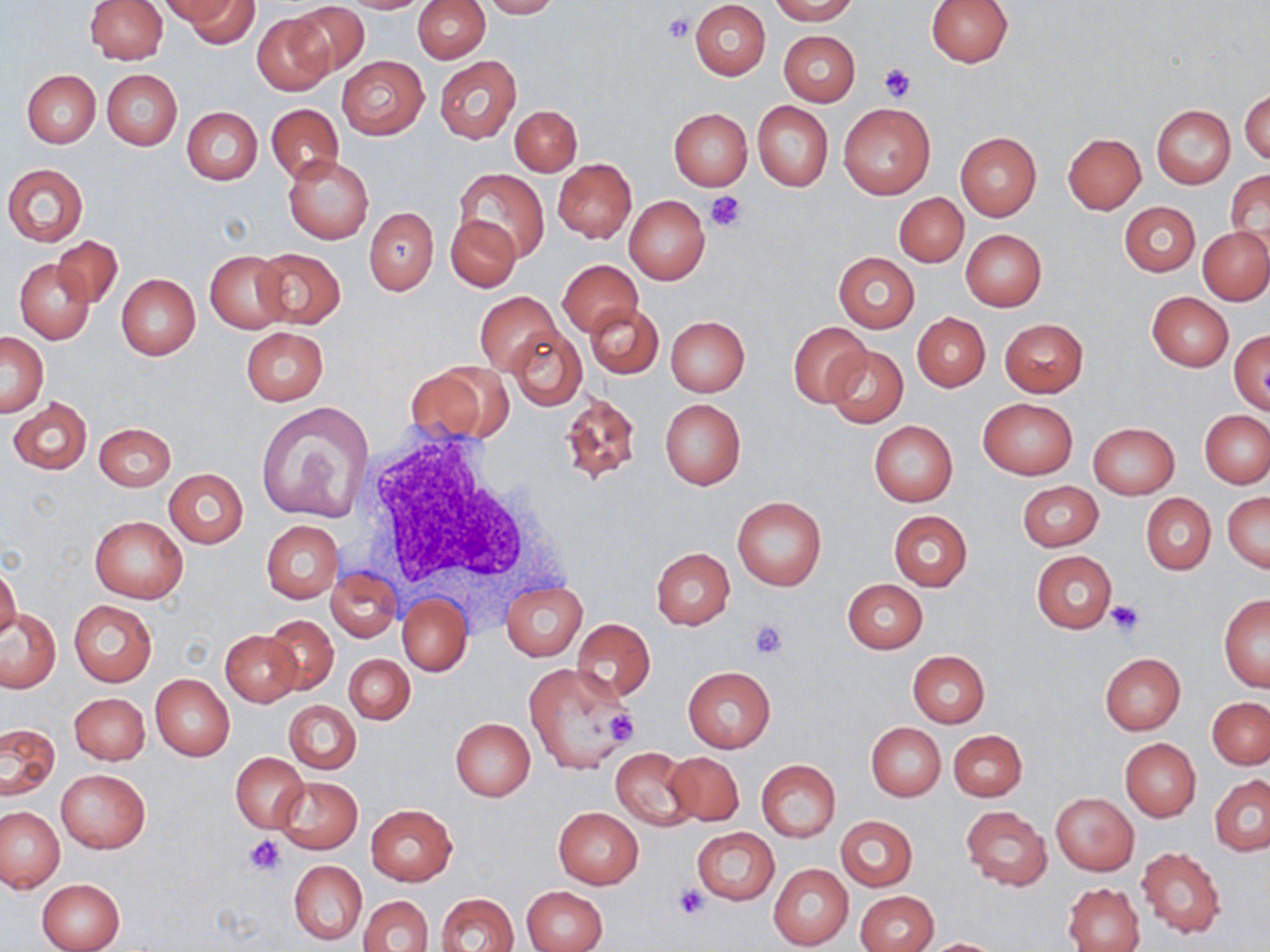

Approximate bounding boxes as (x1, y1, x2, y2) in pixels. White blood cell locations: (359, 428, 543, 607). Uninfected red blood cell locations: (84, 0, 168, 62), (161, 0, 241, 25), (182, 0, 260, 48), (339, 0, 432, 13), (413, 0, 490, 63), (478, 0, 560, 19), (769, 0, 859, 24), (926, 0, 1013, 67), (690, 1, 771, 80), (286, 2, 370, 78), (252, 16, 332, 95), (779, 30, 860, 106), (434, 55, 520, 144), (336, 56, 428, 140), (102, 69, 183, 150), (22, 70, 100, 148), (1240, 88, 1269, 165), (752, 101, 833, 192), (266, 103, 343, 183), (838, 103, 935, 199), (510, 105, 581, 176), (1152, 105, 1234, 189), (182, 107, 262, 185), (669, 108, 751, 190), (955, 132, 1041, 220), (1063, 133, 1145, 214), (282, 152, 374, 244), (552, 159, 636, 243), (3, 163, 89, 246), (454, 169, 549, 261), (1225, 169, 1270, 256), (894, 192, 968, 267), (625, 197, 710, 284), (1120, 201, 1200, 277), (365, 208, 438, 294), (446, 213, 519, 292), (1199, 228, 1270, 304), (961, 229, 1046, 311), (52, 236, 122, 309), (250, 247, 346, 327), (204, 250, 292, 332), (834, 252, 918, 333), (15, 259, 95, 344), (559, 260, 642, 337), (117, 274, 199, 359), (474, 291, 560, 376), (1147, 291, 1234, 371), (585, 304, 663, 378), (912, 314, 990, 390), (665, 315, 751, 396), (1000, 318, 1089, 397), (788, 322, 870, 406), (507, 326, 586, 409), (242, 327, 328, 405), (1229, 330, 1270, 414), (1, 331, 48, 416), (824, 345, 908, 430), (405, 363, 510, 444), (560, 393, 640, 486), (7, 398, 91, 475), (660, 398, 745, 489), (977, 398, 1077, 479), (255, 402, 375, 523), (1200, 411, 1270, 487), (869, 421, 958, 507), (93, 423, 175, 492), (1087, 423, 1179, 500), (164, 468, 248, 547), (1024, 480, 1106, 630), (1017, 481, 1104, 550), (1222, 493, 1269, 572), (1141, 494, 1215, 575), (732, 496, 827, 590), (888, 510, 973, 591), (90, 516, 188, 603), (262, 520, 343, 604), (652, 548, 734, 630), (1032, 551, 1117, 633), (0, 564, 21, 643), (326, 567, 400, 642), (329, 577, 467, 652), (843, 579, 927, 654), (501, 581, 587, 661), (397, 594, 470, 675), (1219, 595, 1270, 690), (69, 600, 157, 687), (0, 608, 60, 692), (263, 614, 339, 696), (571, 619, 656, 701), (220, 629, 299, 705), (907, 650, 990, 727), (345, 653, 415, 725), (1099, 653, 1186, 735), (524, 664, 630, 774), (684, 666, 775, 752), (151, 674, 234, 761), (69, 692, 150, 764), (1208, 698, 1270, 768), (284, 699, 361, 774), (451, 718, 536, 801), (0, 723, 60, 799), (867, 723, 946, 800), (949, 730, 1027, 801), (1120, 738, 1201, 821), (610, 748, 698, 830), (662, 752, 744, 827), (231, 753, 309, 831), (756, 759, 841, 842), (55, 769, 151, 854), (1210, 775, 1270, 855), (274, 776, 363, 853), (1051, 793, 1138, 875), (366, 804, 456, 885), (961, 805, 1052, 891), (0, 806, 66, 893), (553, 807, 643, 888), (836, 816, 918, 890), (691, 827, 779, 904), (1136, 847, 1225, 939), (289, 861, 367, 945), (768, 864, 853, 949), (38, 878, 125, 952), (1063, 882, 1144, 952), (520, 885, 607, 952), (855, 891, 938, 952), (436, 892, 519, 952), (360, 895, 433, 952), (922, 938, 1005, 951). Platelet locations: (665, 13, 694, 42), (878, 64, 917, 103), (706, 192, 748, 232), (1105, 599, 1145, 637), (748, 620, 788, 659), (605, 707, 639, 746), (245, 835, 285, 874), (674, 885, 709, 919). Slide-level diagnosis: no evidence of blood parasites. Optical microscopy. Captured at 1000x magnification. Image is 1270×952 pixels. Thin blood film. May-Grünwald-Giemsa stain. One field of a larger specimen.